Classify this cell by malaria status.
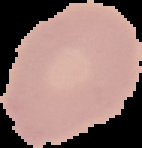

It is uninfected.

The area outside the segmented cell region is set to black. Image is 142×148 pixels. From a thin blood smear.